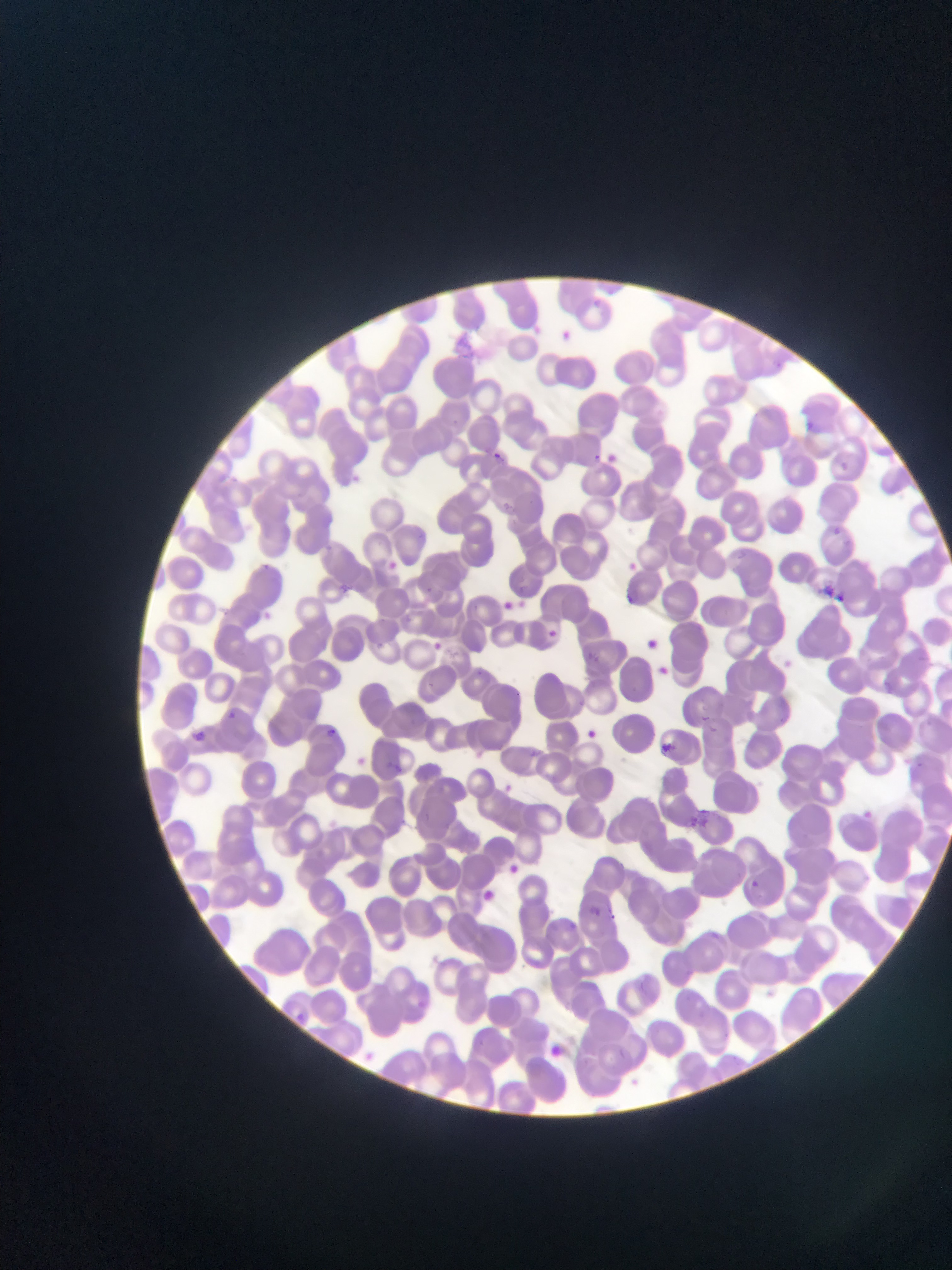

preparation = thin blood film
country = Ghana
Plasmodium parasite locations = approximate bounding boxes as (left, top, right, bottom) in pixels: (561, 321, 585, 344), (808, 421, 817, 433), (592, 446, 623, 463), (492, 449, 510, 470), (835, 459, 856, 482), (827, 523, 853, 542), (258, 552, 275, 569), (621, 557, 648, 583), (385, 558, 406, 573), (339, 583, 359, 594), (822, 585, 839, 600), (628, 590, 644, 604), (494, 594, 515, 609), (508, 595, 537, 616), (257, 606, 269, 620), (544, 626, 570, 649), (643, 635, 660, 647), (431, 642, 443, 651), (585, 649, 606, 669), (659, 665, 667, 679), (226, 710, 238, 720), (325, 724, 337, 739), (585, 726, 595, 740), (194, 730, 218, 746), (663, 737, 681, 758), (528, 745, 549, 762), (388, 761, 405, 772), (501, 779, 522, 796), (686, 806, 712, 830), (863, 808, 875, 822), (506, 862, 518, 872), (746, 878, 756, 895), (477, 890, 495, 902), (592, 903, 619, 922), (544, 1041, 569, 1067)
field of view = single
image size = 952×1270 pixels
capture = mobile-phone photograph through a microscope